State which parasite is depicted.
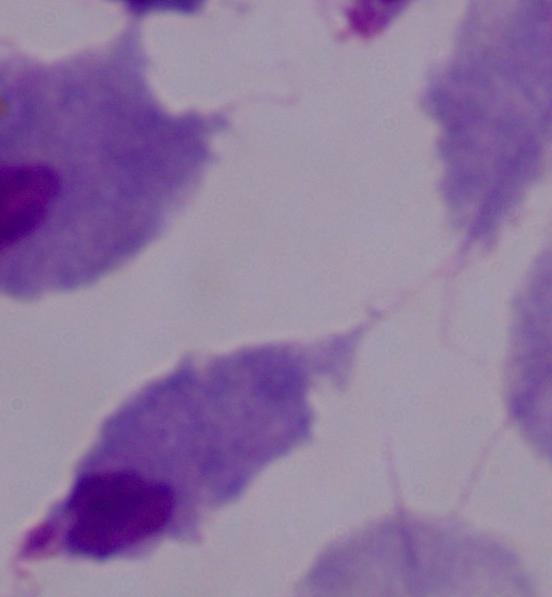

This is a trichomonad.

modality: photomicrograph
magnification: 1000x